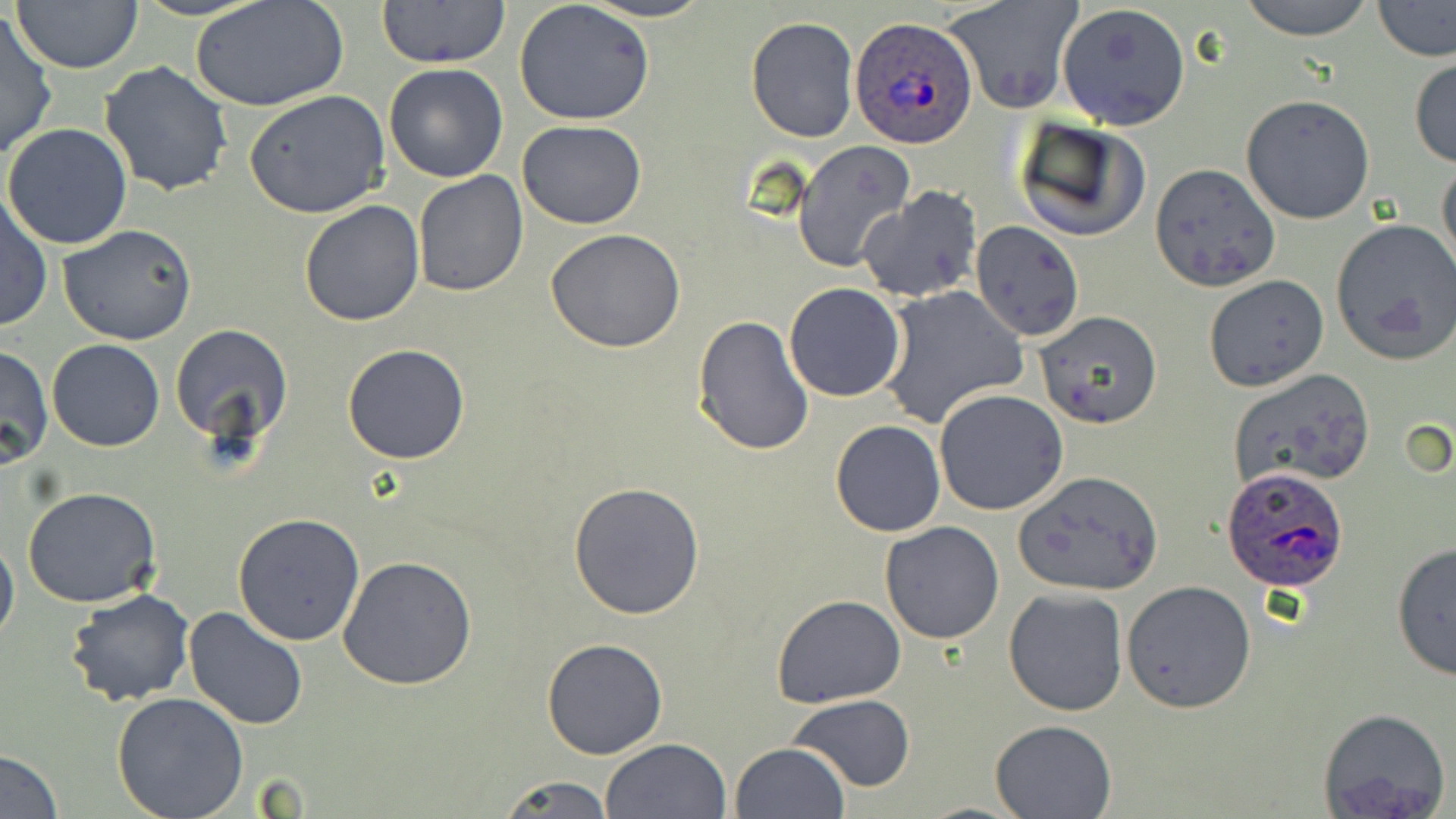

Summary:
  - Coordinate format: approximate bounding boxes as (x1,y1)-(x2,y2) corner pairs in pixels
  - Uninfected red blood cell locations: (12,0)-(145,73), (376,0)-(512,68), (578,0)-(715,23), (945,0)-(1082,115), (1235,0)-(1379,39), (1372,0)-(1455,63), (513,1)-(654,125), (189,2)-(349,113), (1055,3)-(1191,131), (0,10)-(56,161), (745,17)-(858,141), (1409,57)-(1456,168), (101,59)-(235,197), (384,64)-(509,183), (244,90)-(390,219), (1241,95)-(1375,224), (1011,116)-(1150,244), (517,120)-(646,230), (2,123)-(132,249), (795,142)-(915,271), (1436,156)-(1456,276), (1150,163)-(1282,291), (411,171)-(528,296), (857,186)-(982,301), (0,193)-(52,334), (300,199)-(425,327), (971,218)-(1085,342), (1331,220)-(1456,365), (58,224)-(197,346), (546,230)-(687,353), (1202,275)-(1329,392), (783,282)-(907,402), (879,285)-(1027,428), (1034,310)-(1163,429), (692,315)-(814,456), (168,323)-(294,447), (47,339)-(164,452), (0,343)-(52,471), (342,343)-(471,465), (1226,369)-(1377,493), (935,389)-(1069,515), (830,420)-(945,536), (1009,476)-(1158,597), (568,481)-(707,620), (24,488)-(162,607), (233,514)-(365,645), (878,521)-(1004,644), (0,530)-(19,648), (1390,543)-(1455,680), (337,555)-(479,689), (1122,581)-(1256,714), (65,589)-(195,707), (1003,589)-(1128,715), (772,594)-(907,709), (185,607)-(309,732), (540,637)-(668,758), (111,693)-(249,819), (790,693)-(914,793), (1318,708)-(1450,819), (988,719)-(1116,818), (601,738)-(731,819), (729,742)-(850,819), (0,749)-(64,818), (497,774)-(614,817)
  - Plasmodium ovale-infected red blood cell locations: (851,19)-(980,149), (1222,464)-(1352,593)
  - Slide-level diagnosis: Plasmodium ovale
  - Stain: May-Grünwald-Giemsa
  - Modality: light microscopy
  - Preparation: thin blood film
  - Image size: 1456×819 pixels
  - Field of view: single
  - Magnification: 1000x